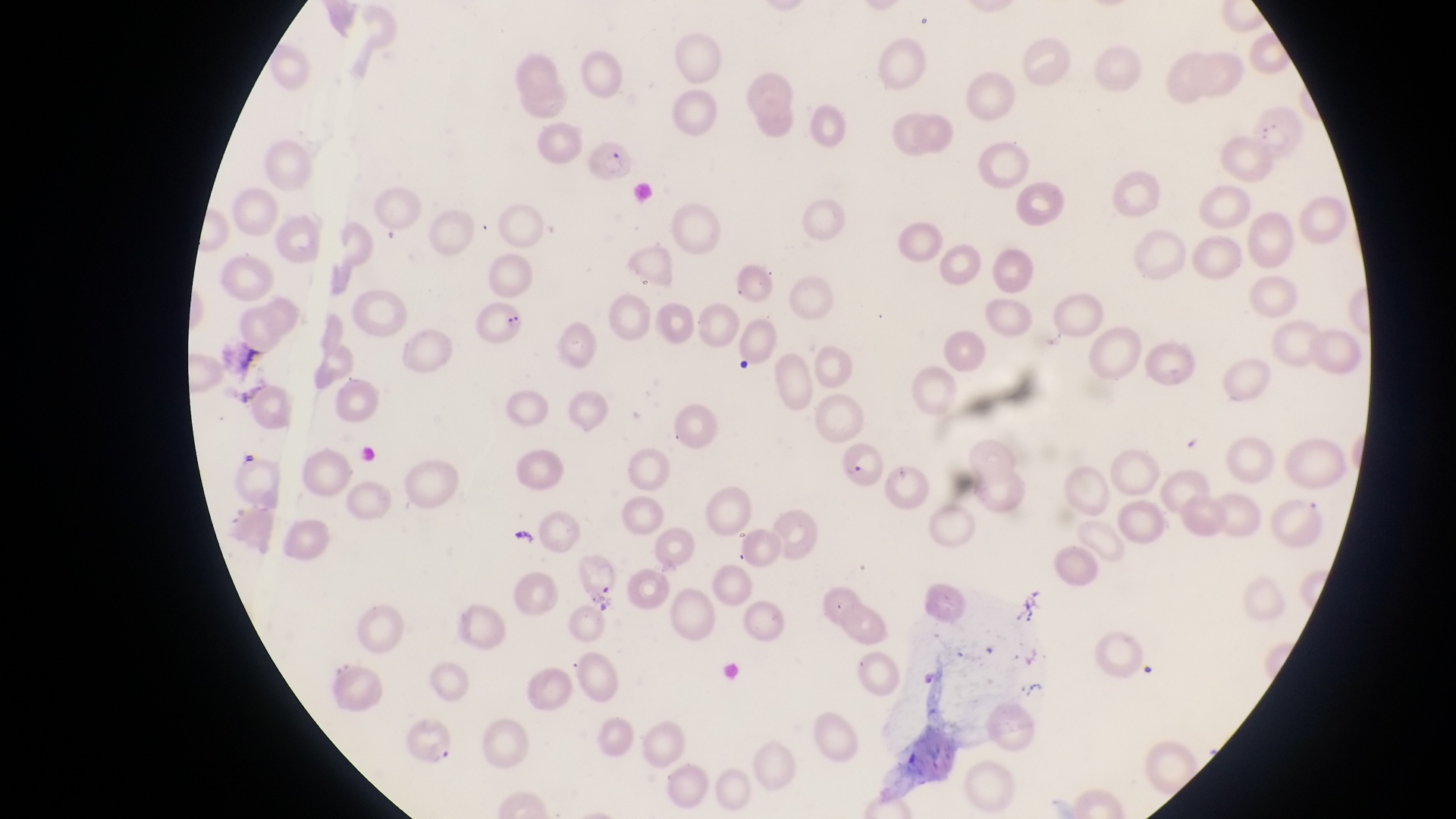
Approximate bounding boxes as {left, top, right, bottom} in pixels. Parasitised red blood cell locations: {585, 139, 637, 189}, {835, 441, 888, 489}. Photographed through the eyepiece of an Olympus CX-23 microscope with a smartphone camera. Thin blood smear. Single field of view. At a magnification of 1000x. Image is 1456×819 pixels. Collected in Uganda.